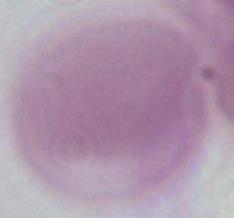
identification = red blood cell
modality = micrograph
magnification = 1000x